Name the blood parasite species.
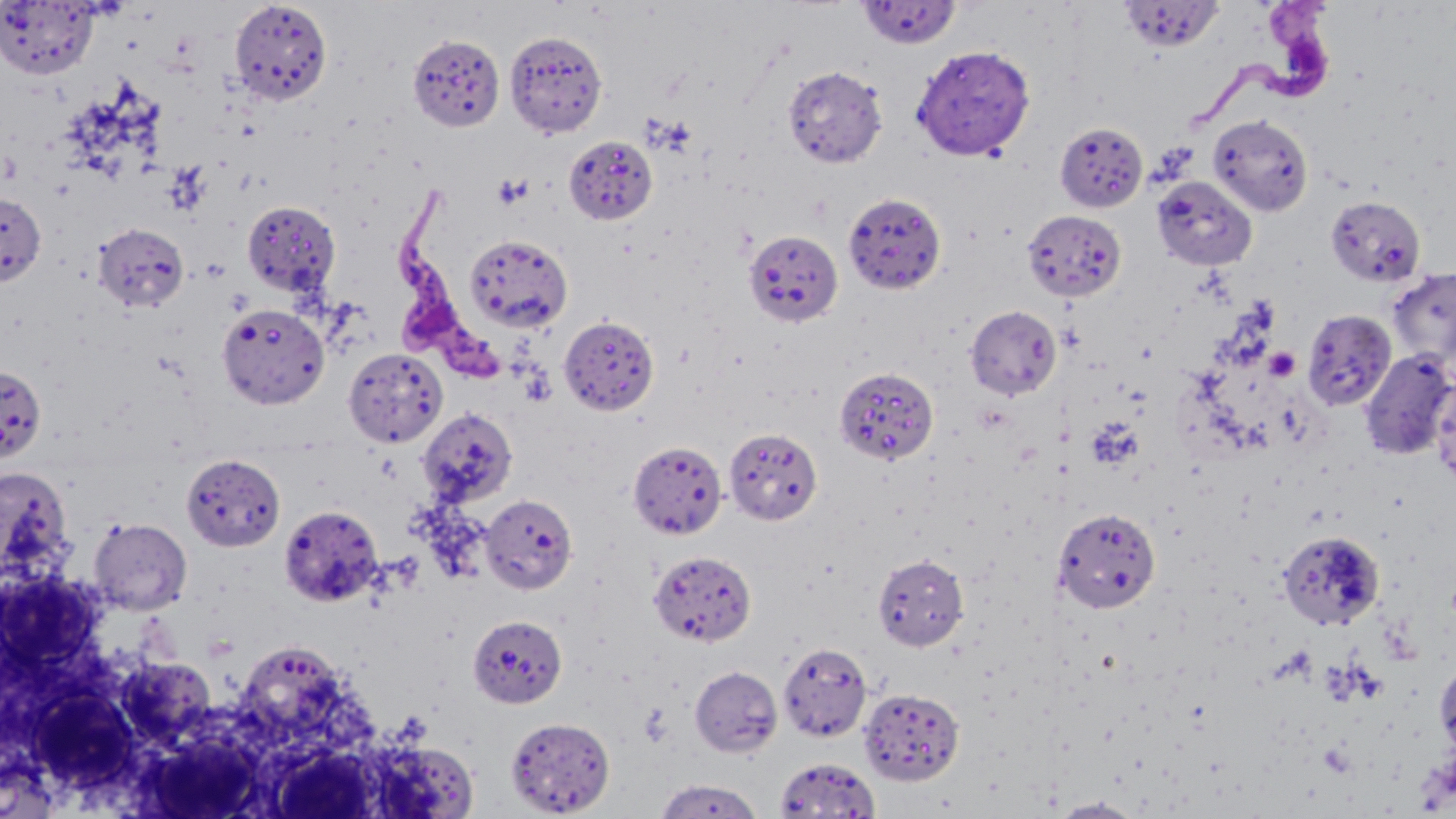

Trypanosoma brucei.

Summary:
  - Coordinate format: approximate bounding boxes as (x1, y1, x2, y2) in pixels
  - Platelet locations: (492, 173, 531, 208), (1264, 346, 1301, 381)
  - Uninfected red blood cell locations: (229, 0, 333, 106), (1, 1, 98, 79), (857, 1, 962, 50), (1120, 1, 1224, 52), (504, 30, 609, 138), (911, 44, 1036, 161), (782, 64, 887, 168), (1208, 114, 1313, 217), (1055, 122, 1148, 212), (564, 135, 658, 225), (1152, 176, 1257, 270), (0, 192, 46, 286), (843, 192, 947, 294), (1325, 196, 1426, 287), (242, 201, 341, 298), (1023, 209, 1126, 301), (92, 222, 189, 312), (744, 229, 843, 327), (464, 234, 573, 332), (1387, 268, 1456, 366), (218, 303, 330, 408), (966, 305, 1062, 399), (1302, 309, 1396, 411), (559, 316, 659, 415), (343, 348, 447, 447), (1359, 350, 1455, 460), (0, 365, 46, 463), (833, 366, 938, 466), (1432, 375, 1456, 489), (417, 407, 517, 507), (724, 426, 823, 526), (628, 440, 727, 539), (181, 454, 285, 551), (0, 465, 76, 585), (480, 494, 578, 594), (279, 504, 384, 606), (1052, 506, 1162, 615), (89, 517, 192, 615), (1278, 531, 1385, 630), (649, 550, 756, 646), (873, 553, 969, 651), (467, 614, 567, 708), (234, 640, 354, 750), (778, 642, 872, 742), (117, 656, 217, 745), (1435, 658, 1456, 759), (689, 665, 783, 758), (27, 685, 142, 790), (858, 687, 964, 785), (506, 717, 615, 816), (371, 740, 480, 815), (270, 744, 382, 818), (775, 756, 880, 818), (654, 777, 764, 818), (1049, 796, 1147, 818)
  - Trypanosoma brucei locations: (1193, 0, 1350, 127), (395, 204, 511, 380)
  - Magnification: 1000x
  - Preparation: thin blood smear
  - Modality: light microscopy
  - Stain: May-Grünwald-Giemsa
  - Image size: 1456×819 pixels
  - Field of view: one of a larger specimen